Assess the morphology of the erythrocytes.
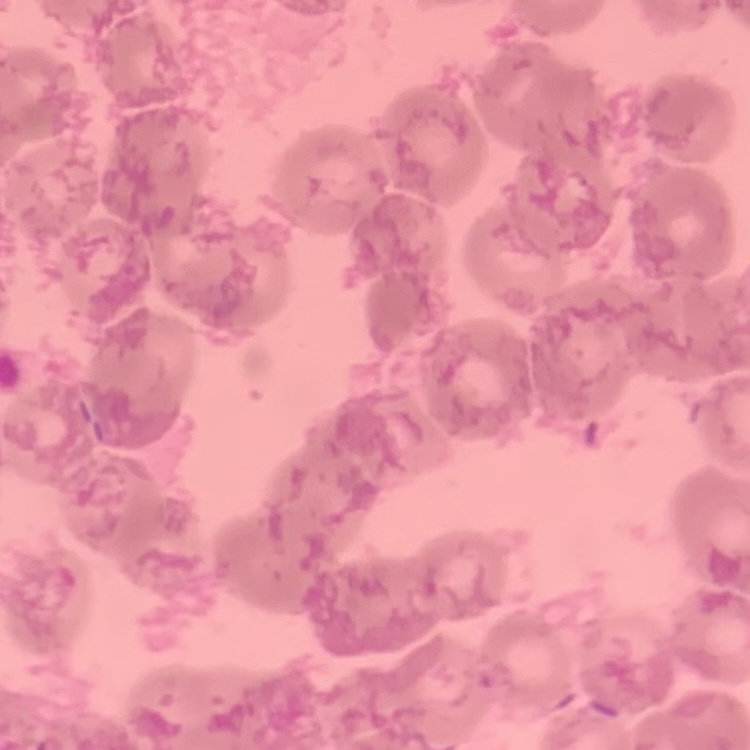

They show rouleaux formation.

Summary:
  - Image type: one tile cut from a larger photomicrograph
  - Stain: Field's or Giemsa
  - Preparation: thin blood smear